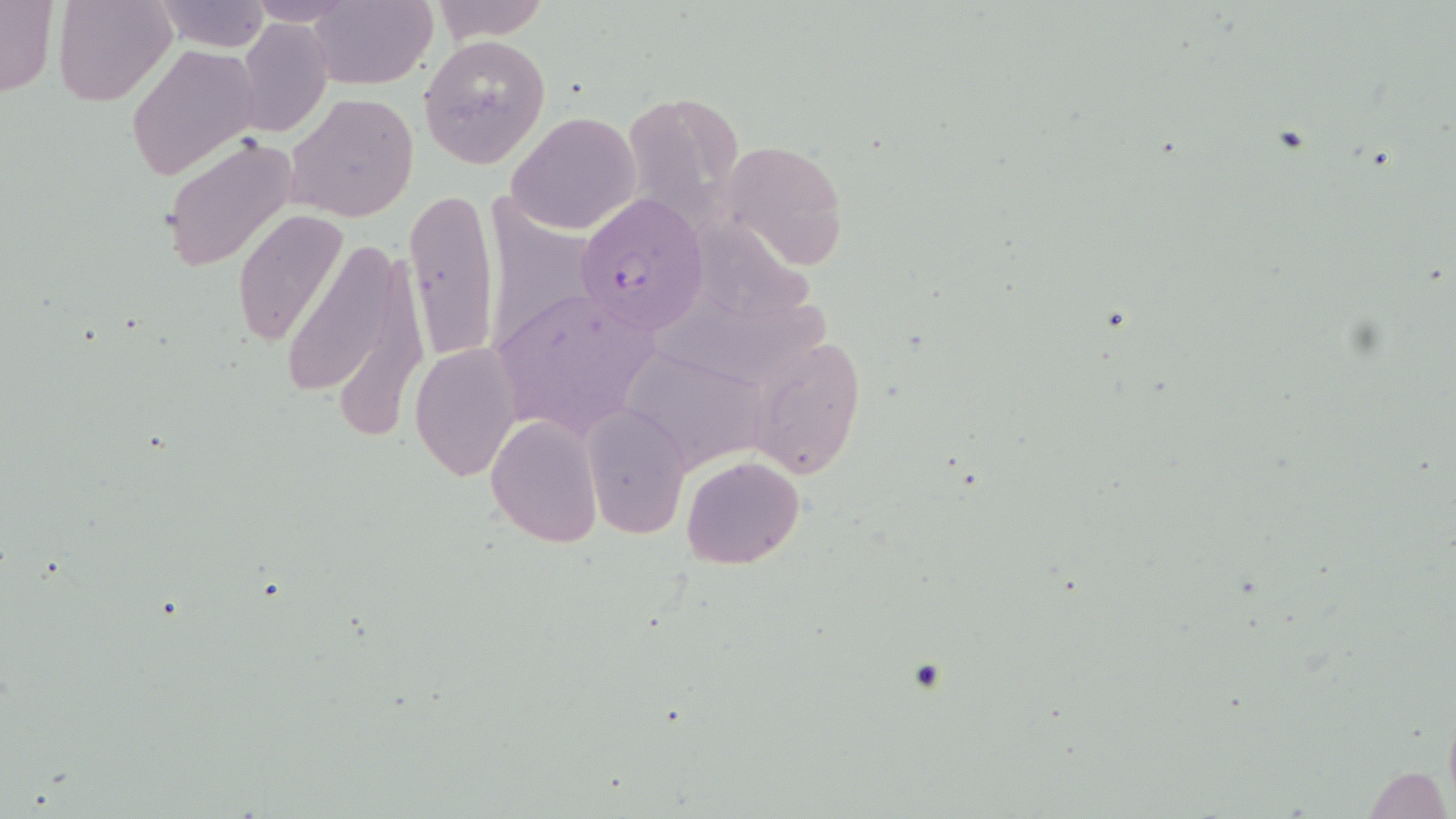 Approximate bounding boxes as (x1,y1)-(x2,y2) corner pairs in pixels. Plasmodium falciparum-infected red blood cell locations: (576,193)-(708,334). Uninfected red blood cell locations: (0,0)-(59,100), (55,0)-(176,106), (245,0)-(359,26), (308,0)-(438,89), (426,0)-(552,42), (152,1)-(269,50), (237,17)-(332,138), (420,34)-(551,169), (126,43)-(261,181), (623,91)-(743,235), (286,93)-(418,224), (505,112)-(641,236), (160,133)-(297,272), (720,138)-(848,272), (487,186)-(595,357), (403,188)-(501,362), (233,209)-(347,346), (701,210)-(828,320), (282,231)-(425,430), (488,285)-(664,443), (665,294)-(838,382), (748,337)-(867,479), (410,343)-(523,481), (618,344)-(774,471), (584,405)-(691,540), (485,416)-(604,549), (682,456)-(804,569), (1364,766)-(1450,819). Slide-level diagnosis: Plasmodium falciparum. Light microscopy. 1000x magnification. Thin blood film. Image is 1456×819 pixels. May-Grünwald-Giemsa-stained preparation. One field of a larger specimen.